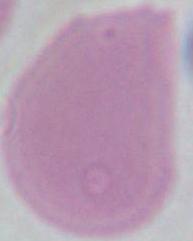

A red blood cell is shown. 1000x magnification. Micrograph.